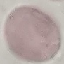
result = negative for malaria parasites
stain = Giemsa
preparation = thin blood film
capture = smartphone through the microscope eyepiece
image type = cell patch, automatically extracted from a larger field of view and resized to 64 × 64 pixels